Classify this cell by malaria status.
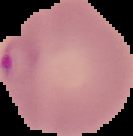

It is parasitized.

image size = 133×136 pixels
preparation = thin blood film
image type = segmented cell region on a black background